State which cell type is depicted.
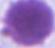

An erythrocyte.

1000x magnification. Photomicrograph.